Comment on the morphology of the erythrocytes.
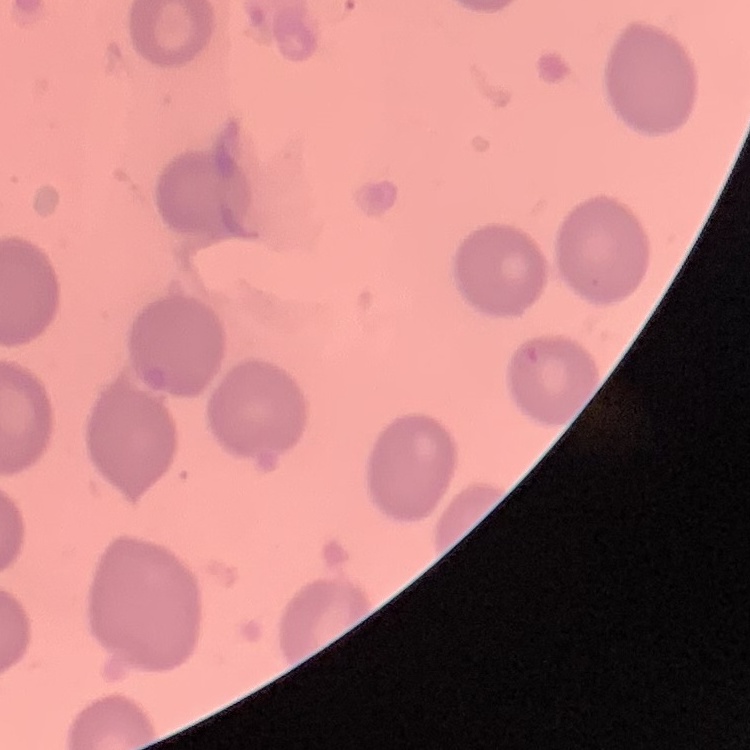

They show no rouleaux formation.

Square crop of a larger photomicrograph. Thin blood film. Stained with either Field's or Giemsa.